Name the cell type shown.
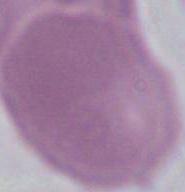
An erythrocyte.

Summary:
  - Modality: micrograph
  - Magnification: 1000x